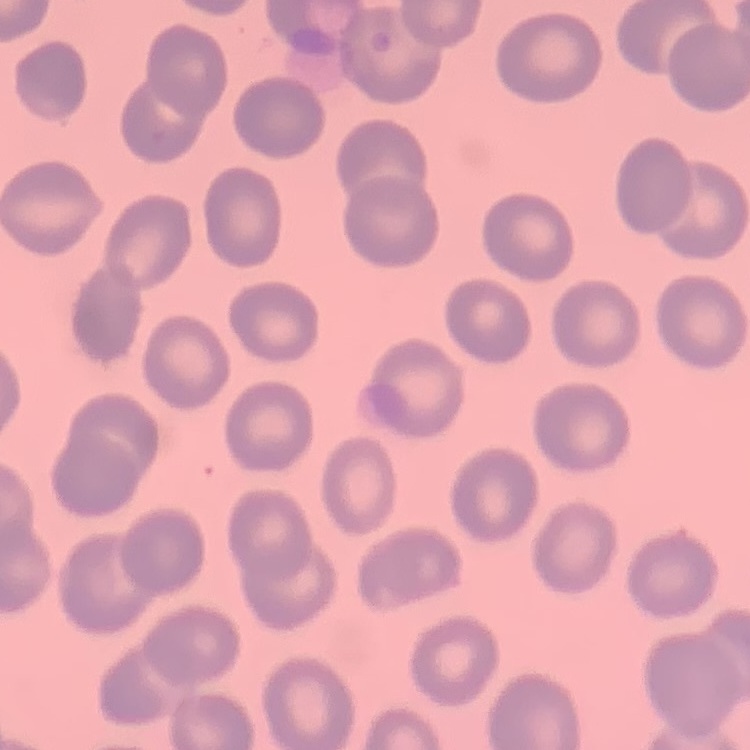

The erythrocytes show no rouleaux formation. Thin blood film. One tile cut from a larger photomicrograph. Field's or Giemsa stain.